Give the preparation type.
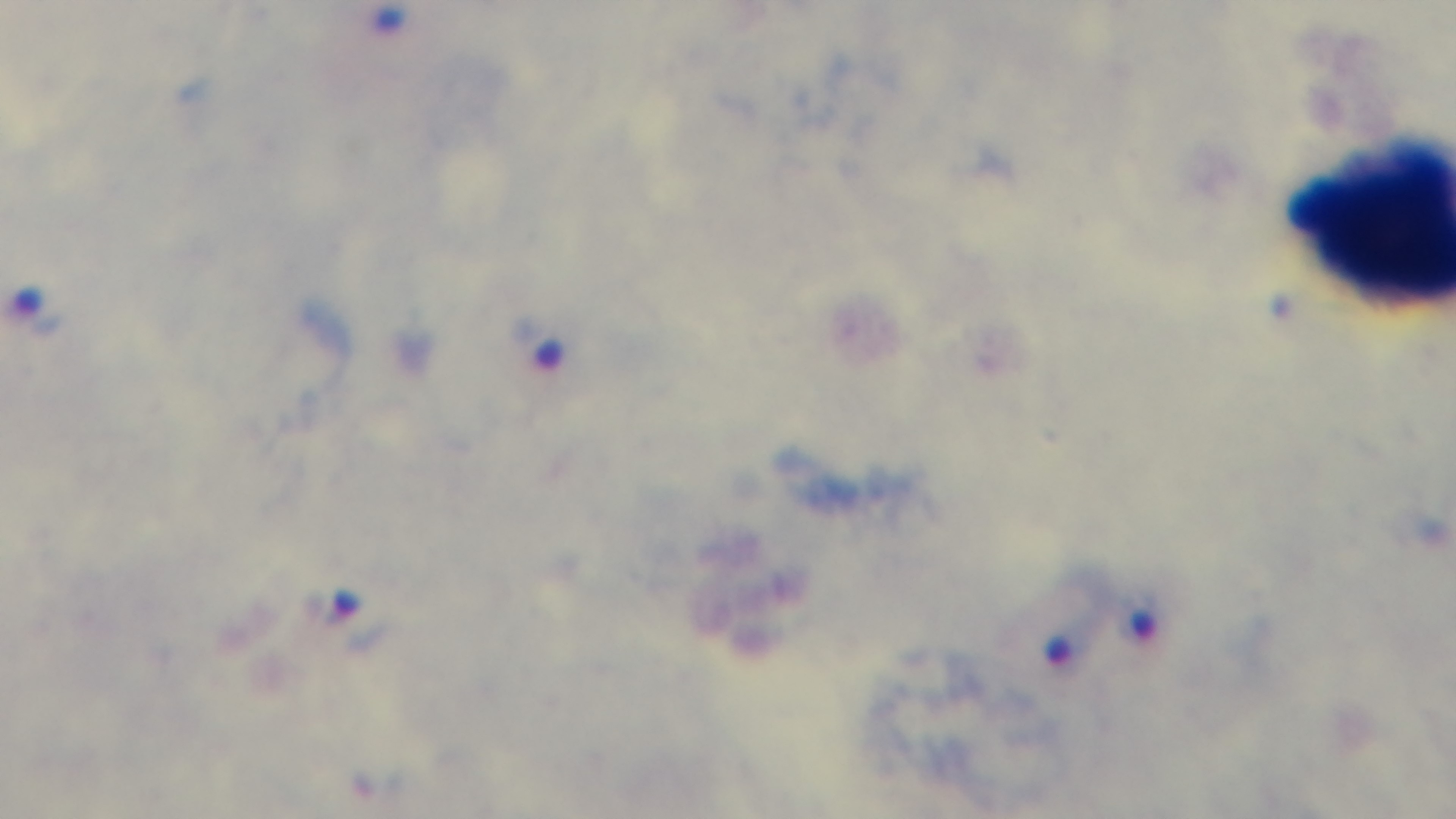

A thick smear.

Summary:
  - Field of view: single
  - Stain: Giemsa
  - Malaria status: infected
  - Capture: mounted 4K digital camera
  - Modality: light microscopy
  - Objective: 100x oil immersion